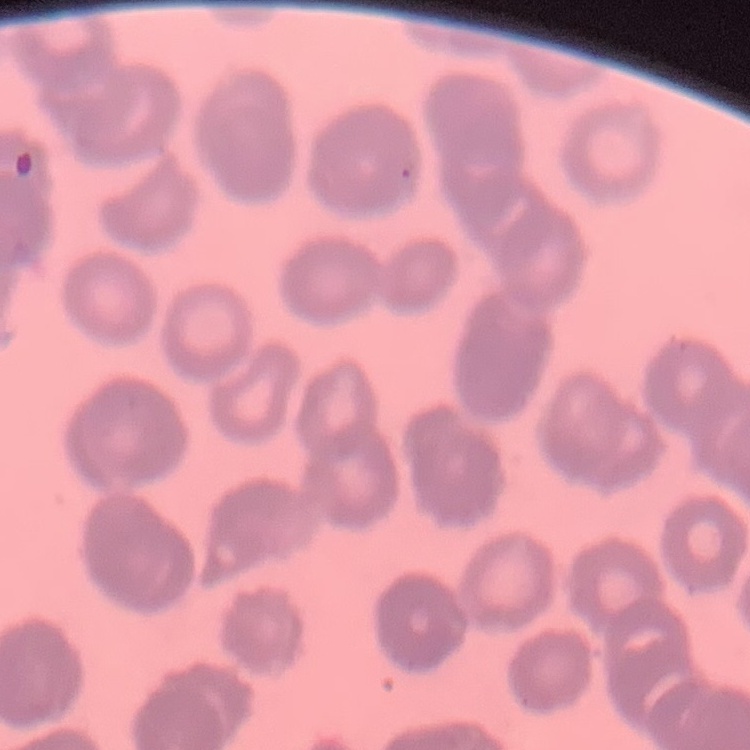

The red blood cells show rouleaux formation. Thin blood film. One tile cut from a larger photomicrograph. Stained with either Field's or Giemsa.